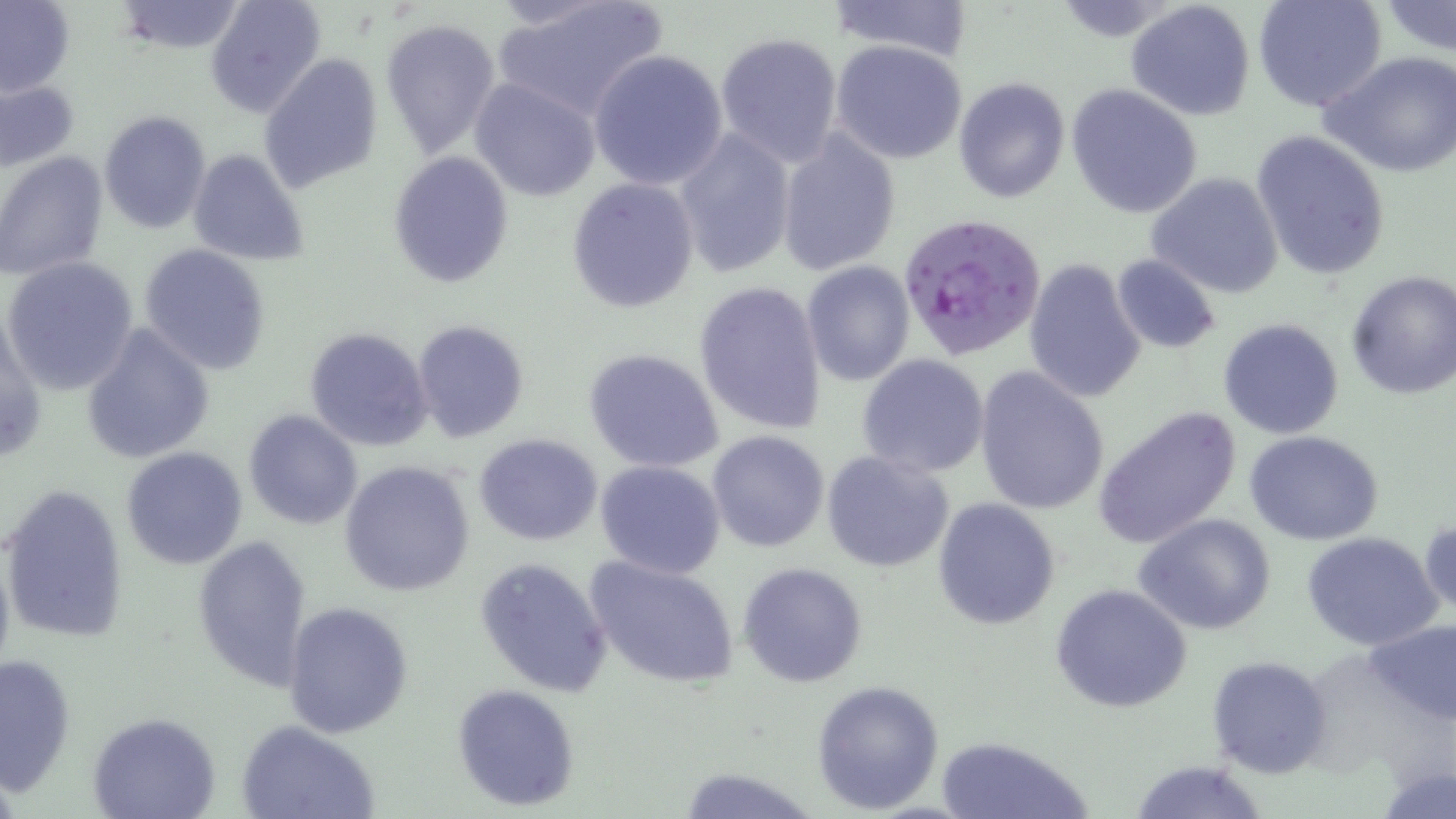
Summary:
  - Coordinate format: approximate bounding boxes as named x1/y1/x2/y2 corners in pixels
  - Plasmodium falciparum-infected red blood cell locations: (x1=898, y1=212, x2=1048, y2=364)
  - Uninfected red blood cell locations: (x1=0, y1=0, x2=75, y2=99), (x1=205, y1=0, x2=327, y2=118), (x1=493, y1=0, x2=667, y2=120), (x1=822, y1=0, x2=978, y2=62), (x1=1125, y1=0, x2=1256, y2=120), (x1=1254, y1=0, x2=1387, y2=112), (x1=1380, y1=0, x2=1456, y2=56), (x1=114, y1=1, x2=246, y2=53), (x1=379, y1=16, x2=501, y2=158), (x1=713, y1=31, x2=844, y2=165), (x1=830, y1=41, x2=969, y2=166), (x1=589, y1=50, x2=729, y2=190), (x1=1319, y1=51, x2=1456, y2=177), (x1=259, y1=55, x2=384, y2=194), (x1=469, y1=77, x2=603, y2=203), (x1=953, y1=78, x2=1071, y2=204), (x1=1, y1=80, x2=79, y2=172), (x1=1067, y1=84, x2=1203, y2=219), (x1=98, y1=110, x2=212, y2=233), (x1=674, y1=128, x2=797, y2=278), (x1=1251, y1=128, x2=1392, y2=280), (x1=776, y1=130, x2=901, y2=276), (x1=188, y1=149, x2=309, y2=265), (x1=387, y1=151, x2=514, y2=288), (x1=0, y1=153, x2=111, y2=281), (x1=1145, y1=171, x2=1285, y2=300), (x1=566, y1=178, x2=698, y2=313), (x1=139, y1=243, x2=271, y2=375), (x1=1112, y1=255, x2=1222, y2=354), (x1=3, y1=257, x2=140, y2=396), (x1=1022, y1=257, x2=1148, y2=405), (x1=802, y1=262, x2=916, y2=386), (x1=1344, y1=271, x2=1456, y2=399), (x1=693, y1=280, x2=829, y2=436), (x1=0, y1=307, x2=45, y2=470), (x1=1217, y1=317, x2=1345, y2=440), (x1=411, y1=319, x2=529, y2=445), (x1=81, y1=324, x2=215, y2=464), (x1=304, y1=325, x2=435, y2=451), (x1=582, y1=348, x2=726, y2=474), (x1=857, y1=353, x2=991, y2=478), (x1=973, y1=366, x2=1110, y2=516), (x1=1094, y1=405, x2=1245, y2=548), (x1=242, y1=409, x2=363, y2=529), (x1=707, y1=430, x2=830, y2=553), (x1=1245, y1=430, x2=1386, y2=545), (x1=473, y1=433, x2=603, y2=545), (x1=120, y1=446, x2=249, y2=571), (x1=821, y1=451, x2=955, y2=573), (x1=340, y1=459, x2=476, y2=597), (x1=595, y1=459, x2=726, y2=580), (x1=3, y1=483, x2=130, y2=643), (x1=933, y1=497, x2=1060, y2=630), (x1=1137, y1=513, x2=1278, y2=637), (x1=1420, y1=516, x2=1455, y2=623), (x1=1301, y1=531, x2=1445, y2=652), (x1=190, y1=532, x2=315, y2=692), (x1=585, y1=555, x2=740, y2=691), (x1=475, y1=557, x2=613, y2=699), (x1=736, y1=561, x2=869, y2=688), (x1=1050, y1=584, x2=1192, y2=715), (x1=284, y1=601, x2=414, y2=739), (x1=1363, y1=617, x2=1456, y2=727), (x1=0, y1=651, x2=76, y2=793), (x1=1206, y1=655, x2=1332, y2=779), (x1=811, y1=679, x2=945, y2=814), (x1=451, y1=683, x2=581, y2=810), (x1=89, y1=712, x2=220, y2=819), (x1=238, y1=718, x2=381, y2=819), (x1=936, y1=735, x2=1094, y2=819), (x1=1126, y1=760, x2=1272, y2=819), (x1=673, y1=763, x2=824, y2=819)
  - Slide-level diagnosis: Plasmodium falciparum
  - Stain: May-Grünwald-Giemsa
  - Modality: optical microscopy
  - Preparation: thin blood smear
  - Magnification: 1000x
  - Image size: 1456×819 pixels
  - Field of view: one of a larger specimen